Give the extent of all uninfected red blood cells.
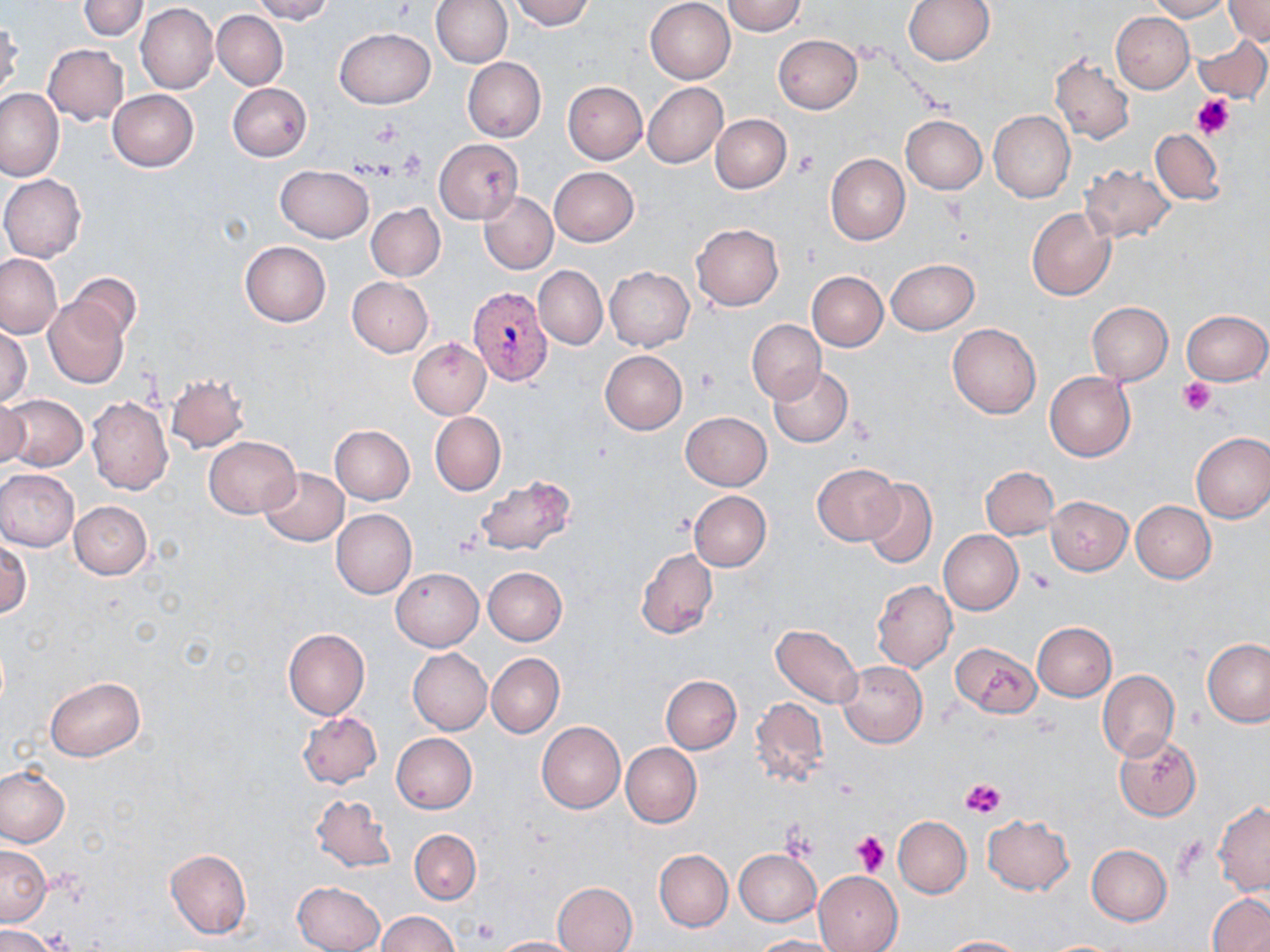

Approximate bounding boxes as [x1, y1, x2, y2] in pixels.
Uninfected red blood cells: [79, 0, 149, 39], [250, 0, 334, 24], [431, 0, 512, 68], [508, 0, 595, 31], [645, 0, 736, 83], [721, 0, 806, 35], [903, 0, 993, 66], [1150, 0, 1229, 21], [1224, 0, 1270, 46], [136, 3, 217, 94], [212, 10, 288, 90], [1111, 12, 1194, 93], [0, 19, 23, 100], [334, 27, 435, 109], [773, 35, 862, 114], [1194, 35, 1270, 103], [42, 43, 128, 125], [1049, 55, 1134, 145], [463, 57, 546, 142], [563, 82, 648, 164], [228, 83, 312, 161], [644, 83, 729, 167], [0, 89, 66, 181], [108, 90, 198, 171], [988, 111, 1075, 202], [710, 114, 791, 192], [900, 115, 987, 194], [1151, 129, 1223, 205], [434, 139, 523, 224], [825, 153, 910, 245], [1081, 163, 1175, 244], [276, 165, 373, 242], [550, 166, 638, 246], [0, 175, 87, 262], [479, 191, 558, 274], [366, 203, 445, 281], [1027, 207, 1116, 301], [691, 223, 784, 311], [240, 241, 331, 326], [0, 253, 63, 340], [886, 259, 979, 334], [534, 266, 607, 350], [604, 266, 695, 351], [805, 271, 888, 352], [70, 274, 140, 342], [347, 276, 433, 356], [42, 296, 130, 389], [1087, 303, 1173, 384], [1182, 309, 1270, 385], [747, 320, 825, 403], [948, 322, 1041, 419], [0, 324, 31, 406], [408, 337, 491, 419], [600, 350, 687, 434], [769, 366, 854, 447], [1044, 371, 1135, 462], [166, 374, 248, 452], [1, 393, 87, 471], [0, 396, 29, 471], [87, 396, 173, 496], [681, 411, 772, 491], [430, 412, 505, 496], [328, 424, 415, 504], [1191, 432, 1270, 524], [203, 436, 299, 518], [812, 463, 902, 545], [259, 466, 349, 546], [981, 467, 1058, 540], [0, 469, 79, 551], [472, 475, 577, 556], [861, 478, 938, 570], [689, 491, 771, 571], [1047, 497, 1131, 574], [69, 500, 152, 578], [1130, 501, 1216, 584], [331, 509, 416, 599], [939, 530, 1023, 616], [0, 542, 31, 619], [636, 547, 718, 639], [483, 566, 567, 644], [391, 567, 483, 650], [871, 580, 957, 672], [1032, 622, 1117, 701], [771, 623, 862, 708], [282, 627, 370, 720], [1203, 638, 1270, 728], [952, 642, 1040, 720], [407, 648, 492, 734], [487, 653, 564, 737], [838, 661, 928, 747], [1098, 670, 1179, 762], [661, 675, 741, 753], [45, 677, 145, 761], [750, 696, 830, 788], [296, 711, 381, 789], [536, 721, 625, 813], [391, 733, 477, 813], [1115, 733, 1202, 820], [621, 743, 702, 827], [0, 765, 70, 846], [310, 794, 396, 873], [1213, 802, 1270, 896], [982, 813, 1073, 895], [893, 816, 971, 897], [409, 829, 480, 904], [0, 843, 51, 925], [1087, 845, 1173, 925], [165, 848, 252, 939], [734, 848, 821, 926], [654, 850, 733, 931], [815, 871, 904, 951], [293, 880, 385, 952], [551, 881, 637, 952], [1208, 893, 1270, 952], [376, 910, 459, 951], [0, 925, 62, 952], [490, 935, 583, 951], [751, 935, 844, 951], [938, 935, 1027, 951].

Summary:
  - Platelet locations: [1191, 94, 1236, 140], [372, 121, 403, 146], [398, 146, 427, 177], [793, 149, 819, 176], [694, 368, 719, 396], [1179, 378, 1213, 416], [1028, 571, 1054, 593], [961, 776, 1006, 818], [781, 828, 819, 858], [851, 832, 890, 875], [469, 916, 501, 945], [37, 928, 77, 951]
  - Plasmodium vivax-infected red blood cell locations: [467, 287, 551, 387]
  - Slide-level diagnosis: Plasmodium vivax
  - Field of view: one of a larger specimen
  - Magnification: 1000x
  - Modality: light microscopy
  - Preparation: thin blood film
  - Stain: May-Grünwald-Giemsa
  - Image size: 1270×952 pixels